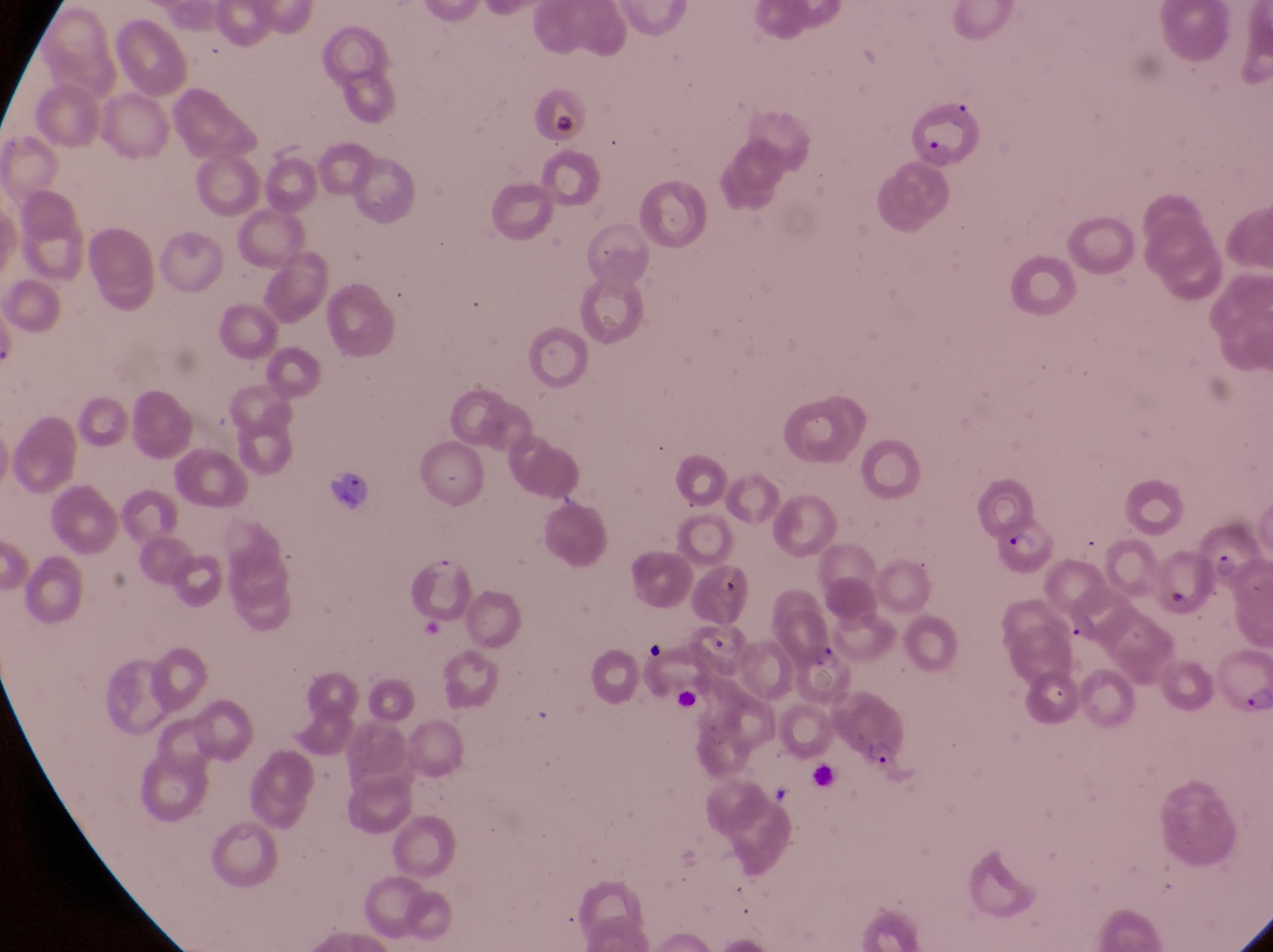
parasitised_red_blood_cell_locations: 'approximate bounding boxes as {left, top, right, bottom} in pixels: {913, 108, 995, 170}, {1193, 519, 1258, 591}, {993, 524, 1067, 584}, {414, 550, 476, 627}, {690, 563, 753, 632}, {1213, 655, 1271, 718}, {842, 702, 909, 772}'
field_of_view: single
magnification: 1000x
preparation: thin blood film
country: Uganda
image_size: 1273×952 pixels
capture: smartphone photograph through the eyepiece of an Olympus CX-23 microscope